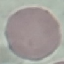

Summary:
  - Result: no malaria parasites detected
  - Image type: automatically extracted cell patch, resized to 64 × 64 pixels
  - Capture: smartphone camera at the microscope eyepiece
  - Stain: Giemsa
  - Preparation: thin blood smear